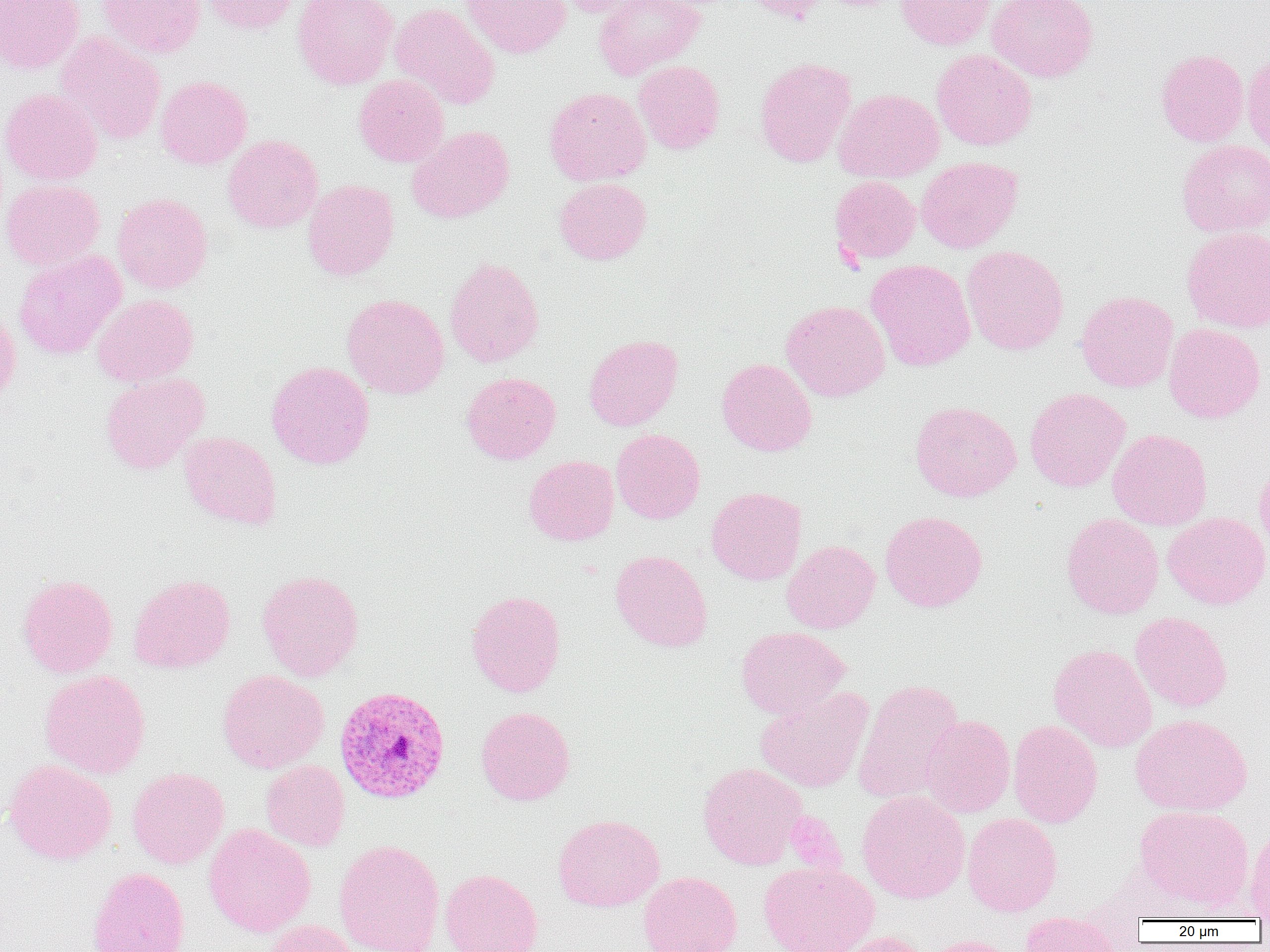
slide-level diagnosis = Plasmodium vivax
modality = light microscopy
image size = 1270×952 pixels
uninfected red blood cell locations = approximate bounding boxes as named x1/y1/x2/y2 corners in pixels: (x1=0, y1=0, x2=84, y2=74), (x1=97, y1=0, x2=206, y2=58), (x1=201, y1=0, x2=299, y2=35), (x1=292, y1=0, x2=399, y2=90), (x1=461, y1=0, x2=571, y2=58), (x1=552, y1=0, x2=644, y2=17), (x1=594, y1=0, x2=706, y2=79), (x1=740, y1=0, x2=831, y2=24), (x1=895, y1=0, x2=996, y2=50), (x1=987, y1=0, x2=1099, y2=82), (x1=390, y1=3, x2=501, y2=110), (x1=56, y1=32, x2=166, y2=145), (x1=931, y1=49, x2=1037, y2=150), (x1=1155, y1=49, x2=1249, y2=147), (x1=1243, y1=50, x2=1270, y2=157), (x1=754, y1=56, x2=857, y2=168), (x1=633, y1=60, x2=725, y2=153), (x1=154, y1=75, x2=253, y2=170), (x1=353, y1=75, x2=450, y2=167), (x1=544, y1=87, x2=651, y2=186), (x1=0, y1=88, x2=103, y2=186), (x1=834, y1=88, x2=944, y2=183), (x1=407, y1=126, x2=515, y2=223), (x1=222, y1=134, x2=324, y2=233), (x1=1177, y1=139, x2=1270, y2=237), (x1=916, y1=157, x2=1022, y2=253), (x1=830, y1=176, x2=920, y2=263), (x1=554, y1=177, x2=651, y2=265), (x1=302, y1=178, x2=399, y2=281), (x1=0, y1=179, x2=106, y2=270), (x1=112, y1=192, x2=213, y2=294), (x1=1182, y1=227, x2=1270, y2=333), (x1=962, y1=245, x2=1068, y2=355), (x1=13, y1=249, x2=126, y2=360), (x1=444, y1=256, x2=544, y2=367), (x1=865, y1=259, x2=975, y2=371), (x1=1076, y1=290, x2=1178, y2=393), (x1=92, y1=294, x2=199, y2=387), (x1=342, y1=294, x2=450, y2=399), (x1=781, y1=300, x2=890, y2=402), (x1=0, y1=302, x2=21, y2=404), (x1=1163, y1=323, x2=1267, y2=424), (x1=583, y1=334, x2=683, y2=431), (x1=716, y1=357, x2=817, y2=457), (x1=266, y1=361, x2=375, y2=469), (x1=100, y1=372, x2=209, y2=473), (x1=461, y1=372, x2=561, y2=465), (x1=1024, y1=387, x2=1131, y2=492), (x1=909, y1=400, x2=1021, y2=502), (x1=611, y1=428, x2=705, y2=524), (x1=1107, y1=429, x2=1213, y2=530), (x1=179, y1=431, x2=282, y2=530), (x1=524, y1=455, x2=619, y2=546), (x1=1254, y1=458, x2=1270, y2=560), (x1=706, y1=487, x2=807, y2=585), (x1=880, y1=511, x2=988, y2=612), (x1=1163, y1=512, x2=1270, y2=610), (x1=1061, y1=513, x2=1164, y2=619), (x1=781, y1=540, x2=880, y2=634), (x1=610, y1=550, x2=713, y2=652), (x1=256, y1=569, x2=364, y2=682), (x1=17, y1=574, x2=118, y2=677), (x1=129, y1=574, x2=236, y2=674), (x1=466, y1=590, x2=566, y2=697), (x1=1130, y1=612, x2=1232, y2=712), (x1=736, y1=626, x2=849, y2=719), (x1=1048, y1=643, x2=1157, y2=753), (x1=39, y1=669, x2=151, y2=779), (x1=216, y1=670, x2=329, y2=773), (x1=853, y1=679, x2=965, y2=804), (x1=754, y1=686, x2=873, y2=793), (x1=475, y1=706, x2=576, y2=806), (x1=1130, y1=713, x2=1253, y2=816), (x1=921, y1=715, x2=1015, y2=818), (x1=1008, y1=719, x2=1103, y2=828), (x1=3, y1=759, x2=117, y2=865), (x1=261, y1=760, x2=350, y2=852), (x1=698, y1=762, x2=807, y2=869), (x1=127, y1=767, x2=229, y2=869), (x1=856, y1=790, x2=971, y2=903), (x1=1134, y1=804, x2=1254, y2=910), (x1=962, y1=813, x2=1063, y2=916), (x1=553, y1=814, x2=665, y2=912), (x1=204, y1=824, x2=316, y2=937), (x1=1246, y1=825, x2=1270, y2=921), (x1=334, y1=840, x2=445, y2=952), (x1=759, y1=860, x2=879, y2=952), (x1=87, y1=867, x2=190, y2=952), (x1=439, y1=868, x2=543, y2=952), (x1=638, y1=871, x2=742, y2=952), (x1=1018, y1=911, x2=1125, y2=952), (x1=264, y1=920, x2=363, y2=952), (x1=835, y1=930, x2=932, y2=952), (x1=918, y1=935, x2=1022, y2=952)
magnification = 1000x
preparation = thin blood film
platelet locations = approximate bounding boxes as named x1/y1/x2/y2 corners in pixels: (x1=784, y1=811, x2=846, y2=875)
field of view = single
Plasmodium vivax-infected red blood cell locations = approximate bounding boxes as named x1/y1/x2/y2 corners in pixels: (x1=334, y1=685, x2=451, y2=805)